Comment on the morphology of the red blood cells.
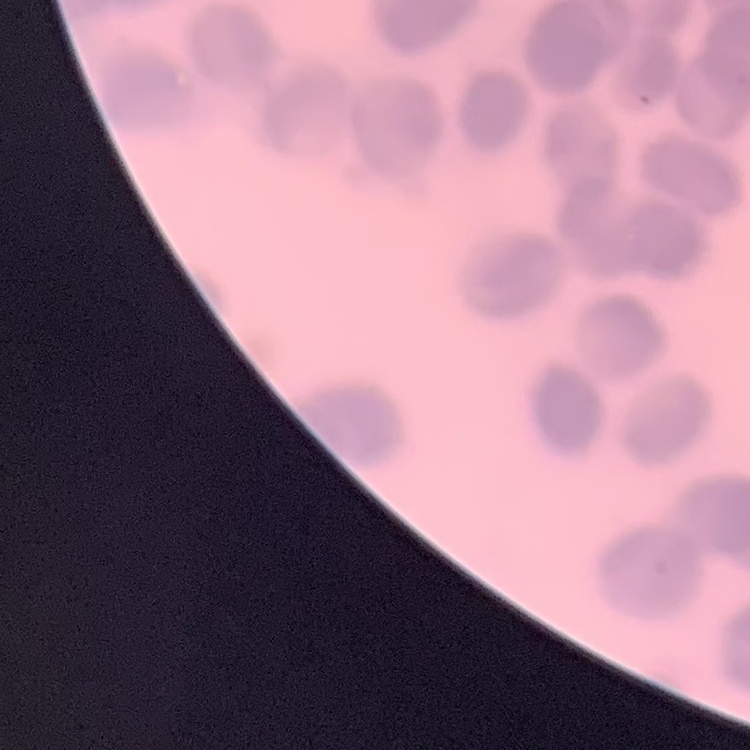
Rouleaux formation.

Square crop of a larger photomicrograph. Thin blood film. Stained with either Field's or Giemsa.